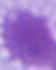 1000x magnification. Micrograph. A red blood cell is seen.